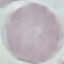

result: no malaria parasites detected
image_type: automatically extracted cell patch, resized to 64 × 64 pixels
stain: Giemsa
preparation: thin blood smear
capture: smartphone camera at the microscope eyepiece